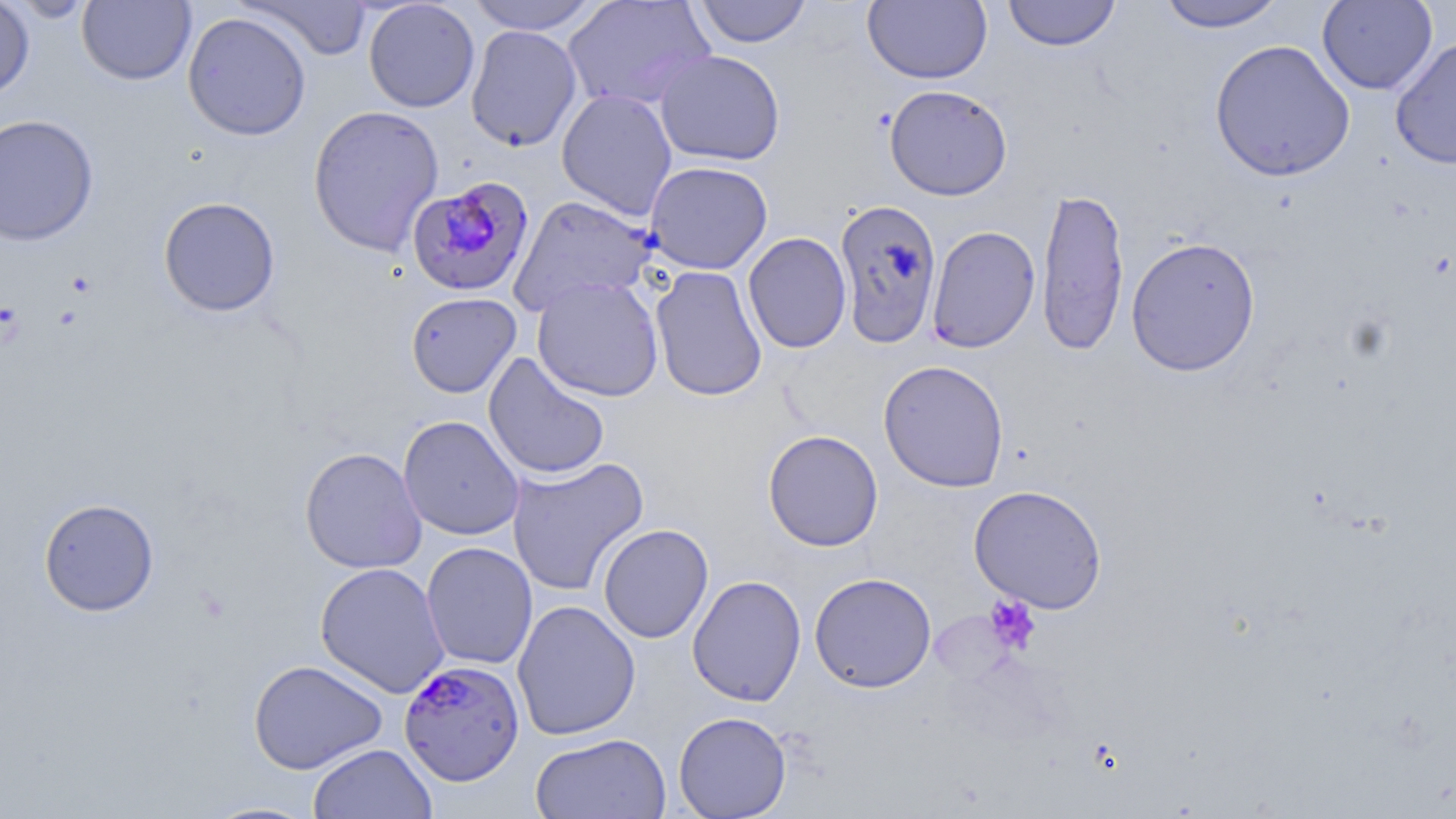

Approximate bounding boxes as named x1/y1/x2/y2 corners in pixels. Uninfected red blood cell locations: (x1=0, y1=0, x2=35, y2=102), (x1=5, y1=0, x2=97, y2=22), (x1=77, y1=0, x2=196, y2=86), (x1=363, y1=0, x2=480, y2=112), (x1=465, y1=0, x2=603, y2=35), (x1=563, y1=0, x2=716, y2=111), (x1=693, y1=0, x2=813, y2=48), (x1=863, y1=0, x2=992, y2=84), (x1=1002, y1=0, x2=1122, y2=51), (x1=1317, y1=0, x2=1437, y2=95), (x1=236, y1=1, x2=373, y2=60), (x1=1155, y1=1, x2=1286, y2=32), (x1=182, y1=11, x2=312, y2=141), (x1=466, y1=25, x2=582, y2=152), (x1=1390, y1=36, x2=1456, y2=170), (x1=1209, y1=39, x2=1356, y2=182), (x1=654, y1=50, x2=786, y2=167), (x1=884, y1=84, x2=1012, y2=201), (x1=556, y1=89, x2=677, y2=221), (x1=307, y1=104, x2=445, y2=256), (x1=0, y1=114, x2=98, y2=246), (x1=645, y1=160, x2=773, y2=275), (x1=1036, y1=186, x2=1128, y2=357), (x1=509, y1=194, x2=659, y2=316), (x1=158, y1=196, x2=280, y2=316), (x1=834, y1=197, x2=943, y2=348), (x1=926, y1=225, x2=1040, y2=353), (x1=743, y1=232, x2=851, y2=353), (x1=1125, y1=236, x2=1261, y2=377), (x1=650, y1=266, x2=768, y2=402), (x1=531, y1=276, x2=664, y2=401), (x1=406, y1=292, x2=521, y2=398), (x1=483, y1=352, x2=610, y2=481), (x1=877, y1=360, x2=1009, y2=492), (x1=398, y1=415, x2=525, y2=540), (x1=763, y1=429, x2=883, y2=552), (x1=300, y1=447, x2=427, y2=574), (x1=507, y1=456, x2=648, y2=596), (x1=968, y1=484, x2=1108, y2=613), (x1=38, y1=497, x2=159, y2=616), (x1=597, y1=523, x2=714, y2=643), (x1=422, y1=542, x2=538, y2=669), (x1=314, y1=562, x2=450, y2=698), (x1=809, y1=572, x2=936, y2=693), (x1=687, y1=575, x2=806, y2=706), (x1=512, y1=599, x2=641, y2=740), (x1=249, y1=659, x2=388, y2=774), (x1=673, y1=711, x2=791, y2=818), (x1=530, y1=732, x2=671, y2=819), (x1=307, y1=743, x2=437, y2=819), (x1=199, y1=800, x2=323, y2=818). Plasmodium falciparum-infected red blood cell locations: (x1=407, y1=177, x2=535, y2=298), (x1=399, y1=659, x2=525, y2=785). Platelet locations: (x1=66, y1=272, x2=96, y2=297), (x1=984, y1=594, x2=1041, y2=654). Slide-level diagnosis: Plasmodium falciparum. Thin blood smear. 1000x magnification. Optical microscopy. May-Grünwald-Giemsa stain. Image is 1456×819 pixels. Single field of view.